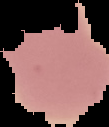
Summary:
  - Preparation: thin blood smear
  - Malaria status: parasitized
  - Image size: 109×127 pixels
  - Image type: cell region segmented out of the field of view; surrounding area masked to black